Locate every Plasmodium falciparum-infected red blood cell.
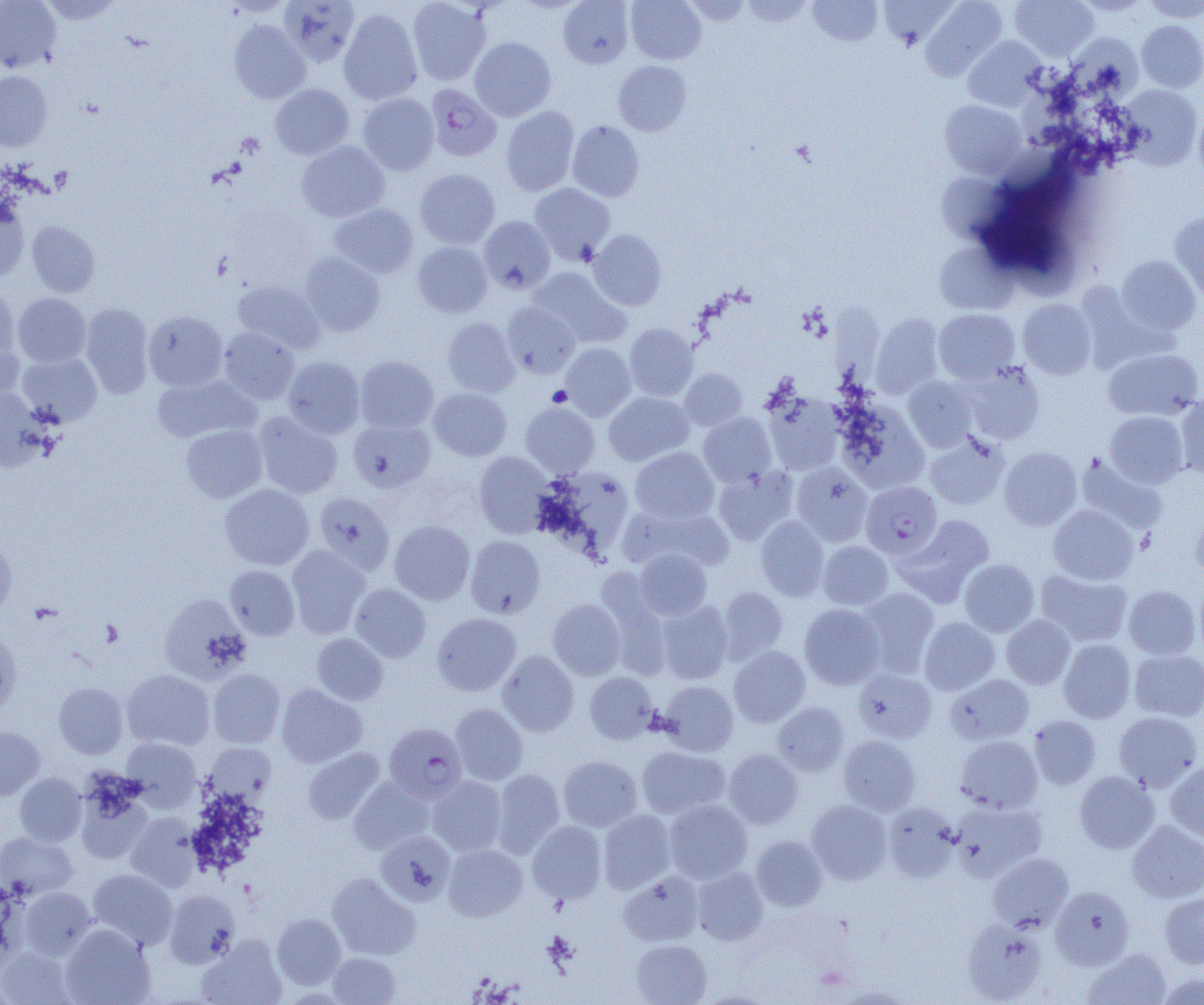
Approximate bounding boxes as (x1, y1, x2, y2) in pixels.
Plasmodium falciparum-infected red blood cells: (425, 84, 501, 162), (861, 481, 942, 559), (384, 723, 467, 803).

Summary:
  - Uninfected red blood cell locations: (0, 0, 61, 73), (39, 0, 123, 25), (279, 0, 360, 67), (407, 0, 490, 85), (558, 0, 634, 68), (626, 0, 706, 64), (683, 0, 751, 25), (741, 0, 812, 27), (808, 0, 882, 47), (920, 0, 1007, 81), (1011, 0, 1099, 61), (1142, 0, 1203, 22), (339, 8, 423, 105), (228, 20, 310, 104), (1137, 20, 1204, 92), (1065, 33, 1143, 100), (962, 36, 1046, 111), (470, 37, 556, 121), (613, 60, 692, 136), (0, 71, 52, 151), (270, 84, 355, 160), (1120, 84, 1202, 169), (357, 93, 439, 175), (940, 100, 1026, 179), (501, 106, 579, 196), (1194, 106, 1204, 187), (567, 120, 644, 202), (296, 140, 390, 222), (415, 169, 500, 249), (938, 173, 1008, 245), (530, 183, 615, 264), (0, 199, 29, 282), (329, 203, 418, 278), (1169, 212, 1204, 303), (479, 216, 556, 294), (27, 221, 99, 297), (588, 229, 667, 310), (412, 242, 492, 318), (934, 242, 1015, 315), (299, 252, 385, 336), (1116, 255, 1200, 337), (528, 267, 629, 347), (233, 280, 325, 353), (0, 281, 18, 361), (13, 293, 91, 367), (1018, 299, 1097, 379), (501, 301, 580, 378), (80, 303, 154, 399), (933, 309, 1020, 384), (143, 311, 228, 391), (870, 313, 943, 398), (442, 317, 518, 397), (624, 323, 698, 401), (218, 328, 300, 404), (0, 338, 25, 407), (560, 343, 636, 421), (1103, 348, 1203, 421), (17, 352, 102, 426), (282, 356, 365, 439), (355, 356, 438, 433), (959, 361, 1045, 445), (680, 368, 747, 430), (151, 374, 260, 443), (904, 376, 978, 451), (0, 387, 49, 472), (429, 388, 511, 461), (762, 391, 844, 475), (604, 392, 693, 466), (1175, 394, 1204, 480), (836, 401, 928, 493), (521, 402, 599, 477), (1105, 411, 1188, 488), (253, 412, 343, 499), (698, 412, 776, 487), (349, 419, 436, 493), (181, 425, 267, 502), (924, 432, 1009, 511), (999, 446, 1082, 530), (630, 447, 719, 524), (474, 452, 551, 537), (1075, 453, 1168, 535), (791, 462, 872, 546), (713, 467, 797, 545), (219, 484, 314, 570), (314, 492, 394, 574), (620, 505, 735, 573), (1048, 505, 1139, 585), (1190, 510, 1204, 579), (896, 515, 994, 605), (756, 516, 829, 601), (389, 520, 475, 605), (0, 535, 17, 617), (465, 536, 545, 618), (818, 541, 893, 610), (286, 545, 370, 638), (634, 549, 712, 620), (960, 559, 1039, 636), (225, 565, 300, 640), (1037, 570, 1133, 647), (598, 581, 672, 679), (351, 583, 431, 663), (1123, 585, 1201, 660), (719, 586, 788, 664), (857, 587, 940, 678), (159, 595, 251, 683), (548, 599, 625, 680), (655, 600, 734, 684), (799, 604, 885, 690), (432, 613, 521, 696), (1002, 615, 1075, 688), (919, 617, 1000, 695), (0, 630, 21, 714), (311, 633, 388, 705), (1058, 639, 1136, 723), (728, 646, 810, 727), (1129, 649, 1204, 721), (498, 650, 579, 735), (208, 668, 285, 748), (854, 668, 937, 743), (122, 669, 215, 751), (584, 671, 658, 745), (945, 674, 1034, 745), (658, 681, 738, 756), (54, 682, 128, 759), (276, 684, 367, 768), (773, 702, 849, 776), (450, 703, 528, 785), (1113, 711, 1202, 791), (1029, 715, 1101, 789), (0, 726, 45, 800), (838, 735, 921, 815), (955, 735, 1043, 813), (122, 738, 202, 810), (204, 742, 276, 803), (636, 746, 730, 820), (302, 747, 385, 825), (723, 749, 803, 829), (558, 755, 642, 832), (1165, 760, 1204, 843), (491, 769, 565, 857), (1074, 770, 1159, 854), (15, 773, 86, 847), (427, 775, 508, 856), (349, 777, 433, 853), (74, 779, 154, 864), (664, 799, 753, 884), (807, 800, 892, 884), (949, 800, 1048, 883), (882, 802, 960, 882), (598, 810, 676, 894), (126, 812, 203, 891), (527, 820, 607, 903), (1127, 820, 1204, 903), (0, 831, 79, 900), (376, 831, 455, 905), (750, 835, 827, 911), (443, 843, 527, 921), (987, 852, 1074, 932), (691, 866, 768, 945), (87, 869, 178, 950), (619, 871, 704, 946), (327, 873, 420, 960), (1050, 885, 1134, 970), (18, 886, 96, 960), (164, 890, 240, 968), (1160, 890, 1204, 968), (272, 913, 346, 989), (962, 918, 1047, 1003), (60, 924, 155, 1005), (199, 934, 288, 1005), (631, 939, 713, 1005), (0, 945, 76, 1004), (1082, 948, 1171, 1005), (328, 952, 400, 1004), (1157, 972, 1204, 1005)
  - Platelet locations: (548, 386, 572, 407), (99, 620, 123, 646)
  - Slide-level diagnosis: Plasmodium falciparum
  - Image size: 1204×1005 pixels
  - Preparation: thin blood film
  - Magnification: 1000x
  - Modality: light microscopy
  - Field of view: one of a larger specimen